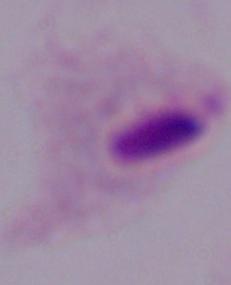
Summary:
  - Identification: trichomonad
  - Magnification: 1000x
  - Modality: micrograph